Locate every malaria parasite.
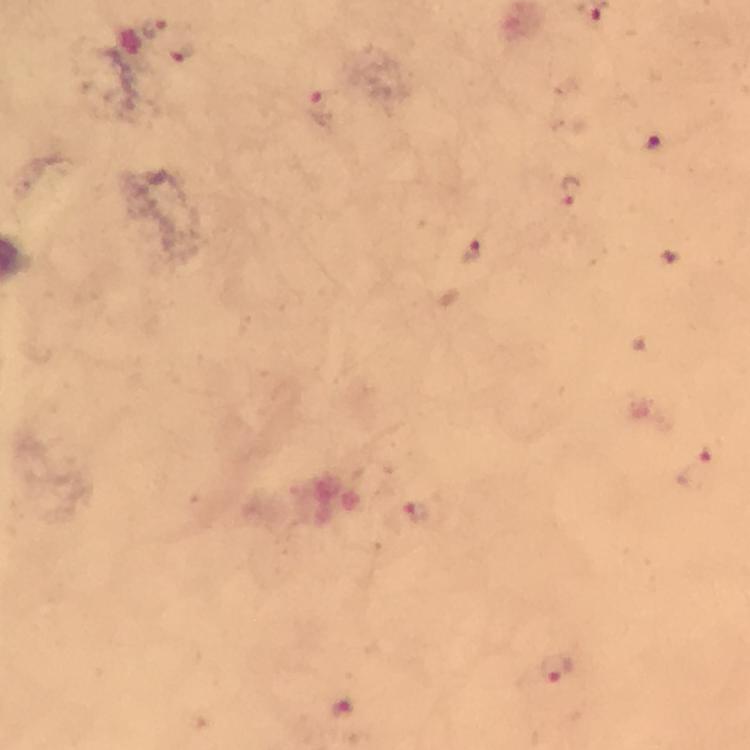
Approximate centers as {x, y} in pixels.
Malaria parasites: {154, 28}, {181, 52}, {322, 110}, {651, 145}, {571, 189}, {473, 252}, {709, 454}, {417, 512}, {556, 668}, {340, 708}.

Summary:
  - Cropped from: a single field of view
  - Preparation: thick blood smear
  - Immersion oil: applied
  - Stain: Giemsa
  - Capture: smartphone mounted on the microscope
  - Context: from a malaria diagnostic workup
  - Image size: 750×750 pixels
  - Magnification: 100x